Outline each Plasmodium falciparum-infected red blood cell.
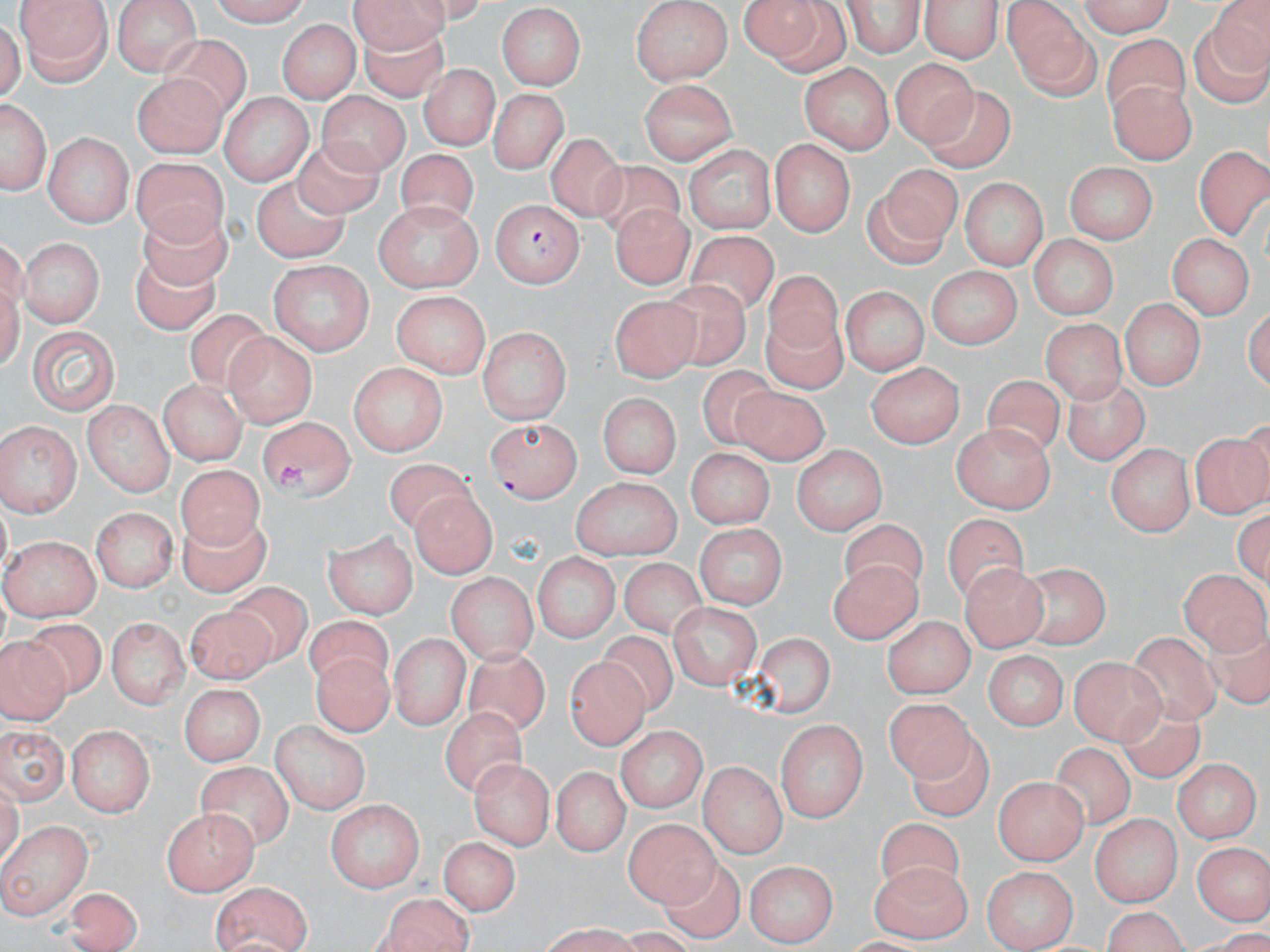
Approximate bounding boxes as [x1, y1, x2, y2] in pixels.
Plasmodium falciparum-infected red blood cells: [490, 197, 583, 286].

Uninfected red blood cell locations: [15, 0, 116, 82], [112, 0, 202, 76], [206, 0, 311, 24], [351, 0, 451, 47], [737, 0, 845, 70], [919, 0, 1007, 62], [1072, 0, 1174, 39], [634, 1, 731, 84], [841, 3, 925, 59], [496, 4, 586, 90], [1004, 4, 1102, 100], [1189, 8, 1270, 105], [277, 17, 361, 105], [357, 21, 451, 102], [1098, 32, 1191, 116], [159, 34, 247, 125], [893, 57, 977, 148], [803, 63, 893, 154], [424, 66, 495, 149], [131, 72, 227, 155], [642, 78, 738, 163], [1110, 79, 1194, 166], [486, 89, 569, 172], [916, 89, 1015, 173], [222, 90, 310, 184], [324, 95, 409, 171], [0, 96, 51, 191], [43, 131, 132, 224], [546, 134, 626, 222], [294, 137, 387, 220], [770, 138, 857, 235], [683, 145, 779, 233], [1193, 146, 1269, 234], [399, 148, 481, 224], [132, 154, 228, 248], [590, 162, 682, 238], [866, 162, 961, 261], [1065, 162, 1156, 243], [249, 177, 349, 262], [958, 178, 1048, 266], [375, 203, 486, 291], [137, 204, 239, 292], [617, 209, 691, 285], [686, 231, 777, 317], [1166, 234, 1253, 320], [1028, 235, 1118, 322], [18, 239, 101, 327], [129, 250, 223, 338], [265, 258, 376, 355], [924, 265, 1023, 347], [762, 272, 845, 357], [666, 279, 752, 367], [842, 284, 927, 378], [391, 289, 492, 379], [610, 293, 700, 377], [1119, 297, 1202, 390], [759, 305, 847, 390], [184, 310, 274, 392], [1042, 316, 1122, 404], [27, 323, 120, 415], [478, 327, 567, 425], [225, 330, 317, 426], [866, 359, 965, 448], [351, 362, 449, 454], [696, 366, 776, 452], [979, 375, 1066, 460], [1066, 378, 1149, 465], [161, 380, 246, 465], [728, 386, 828, 465], [595, 392, 681, 481], [85, 399, 173, 492], [484, 417, 584, 499], [258, 418, 355, 498], [0, 422, 78, 519], [950, 423, 1057, 514], [1187, 435, 1269, 516], [1108, 442, 1194, 537], [685, 446, 771, 527], [796, 448, 885, 535], [175, 464, 264, 553], [573, 478, 680, 556], [412, 493, 496, 580], [91, 506, 176, 591], [183, 508, 268, 598], [941, 515, 1028, 603], [836, 519, 933, 588], [695, 524, 785, 612], [323, 531, 416, 617], [0, 536, 99, 618], [533, 553, 620, 646], [617, 554, 712, 645], [827, 557, 922, 646], [1021, 562, 1109, 647], [962, 564, 1048, 647], [1181, 570, 1268, 661], [450, 577, 535, 664], [227, 578, 310, 665], [185, 603, 271, 685], [667, 603, 757, 686], [882, 614, 970, 700], [303, 616, 402, 689], [108, 617, 187, 706], [29, 618, 105, 698], [1201, 619, 1270, 711], [602, 628, 685, 717], [754, 628, 835, 720], [1124, 628, 1221, 727], [393, 634, 465, 730], [3, 636, 61, 721], [310, 648, 396, 737], [469, 649, 550, 739], [984, 653, 1066, 733], [1071, 655, 1161, 741], [567, 656, 648, 753], [179, 682, 266, 766], [1115, 696, 1204, 787], [875, 699, 978, 788], [445, 700, 535, 804], [776, 718, 869, 824], [265, 723, 371, 811], [616, 725, 705, 811], [0, 726, 70, 800], [912, 726, 993, 819], [68, 727, 150, 816], [1051, 746, 1132, 828], [471, 757, 552, 851], [1173, 760, 1257, 841], [192, 762, 297, 851], [701, 762, 785, 858], [549, 765, 631, 855], [1187, 771, 1267, 906], [994, 774, 1088, 865], [326, 797, 423, 889], [161, 808, 258, 895], [623, 813, 716, 906], [1088, 814, 1179, 903], [0, 819, 92, 919], [879, 821, 960, 899], [437, 837, 523, 913], [1194, 841, 1268, 926], [654, 855, 741, 932], [745, 857, 837, 946], [868, 860, 973, 937], [986, 860, 1078, 943], [67, 881, 142, 952], [207, 883, 313, 952], [369, 893, 475, 952]. Slide-level diagnosis: Plasmodium falciparum. May-Grünwald-Giemsa stain. Light microscopy. Single field of view. Thin blood smear. Captured at 1000x magnification. Image is 1270×952 pixels.